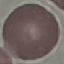
Summary:
  - Malaria status: uninfected
  - Capture: smartphone through the microscope eyepiece
  - Preparation: thin blood smear
  - Image type: cell patch, automatically extracted from a larger field of view and resized to 64 × 64 pixels
  - Stain: Giemsa